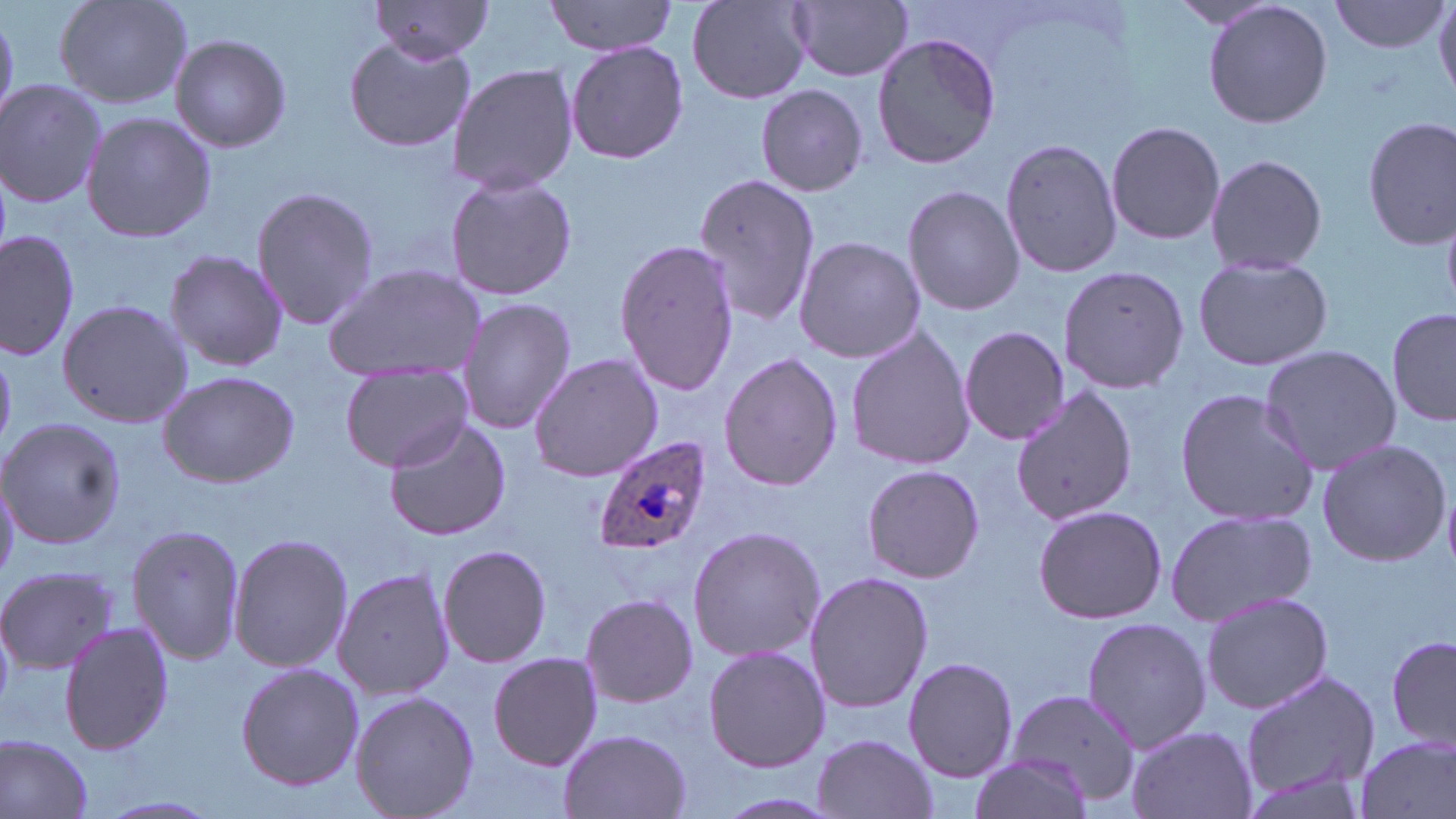
Plasmodium ovale-infected red blood cell locations = approximate bounding boxes as (x1, y1, x2, y2) in pixels: (591, 436, 717, 558)
slide-level diagnosis = Plasmodium ovale
image size = 1456×819 pixels
magnification = 1000x
field of view = single
preparation = thin blood smear
stain = May-Grünwald-Giemsa
modality = optical microscopy
uninfected red blood cell locations = approximate bounding boxes as (x1, y1, x2, y2) in pixels: (53, 0, 192, 109), (544, 0, 681, 56), (1202, 0, 1334, 130), (1329, 0, 1450, 55), (789, 1, 914, 82), (369, 2, 499, 62), (687, 2, 812, 104), (1431, 3, 1456, 96), (871, 29, 1001, 172), (169, 32, 292, 153), (345, 35, 478, 154), (565, 41, 692, 167), (445, 61, 580, 196), (0, 78, 107, 210), (757, 84, 870, 199), (81, 112, 217, 245), (1361, 114, 1456, 247), (1106, 120, 1227, 246), (999, 136, 1124, 280), (1205, 152, 1328, 276), (444, 172, 579, 302), (693, 172, 820, 330), (251, 184, 378, 330), (902, 184, 1025, 318), (1, 228, 81, 363), (792, 235, 925, 362), (615, 238, 739, 398), (166, 250, 289, 373), (1191, 252, 1335, 371), (1057, 260, 1190, 393), (321, 263, 489, 382), (56, 296, 193, 428), (456, 297, 578, 434), (1387, 307, 1454, 429), (959, 324, 1069, 447), (844, 325, 976, 472), (1259, 343, 1400, 473), (719, 351, 844, 492), (527, 352, 663, 482), (340, 365, 474, 472), (156, 369, 301, 490), (1173, 386, 1321, 526), (1009, 387, 1138, 526), (1, 416, 126, 549), (382, 417, 513, 541), (1315, 436, 1452, 569), (861, 464, 986, 584), (1, 471, 20, 584), (1032, 504, 1168, 625), (1165, 509, 1317, 626), (127, 524, 245, 666), (687, 524, 825, 663), (229, 529, 353, 675), (437, 543, 553, 668), (0, 564, 117, 672), (333, 568, 453, 701), (804, 570, 933, 713), (1200, 590, 1333, 715), (577, 593, 700, 711), (1081, 616, 1210, 754), (61, 621, 173, 755), (1386, 634, 1456, 749), (703, 645, 832, 772), (488, 652, 606, 771), (903, 656, 1019, 783), (235, 662, 365, 791), (1240, 666, 1384, 803), (349, 690, 479, 819), (1003, 690, 1140, 807), (1125, 725, 1257, 819), (556, 729, 693, 819), (1353, 733, 1455, 819), (0, 734, 95, 819), (811, 734, 938, 819), (969, 753, 1095, 819)